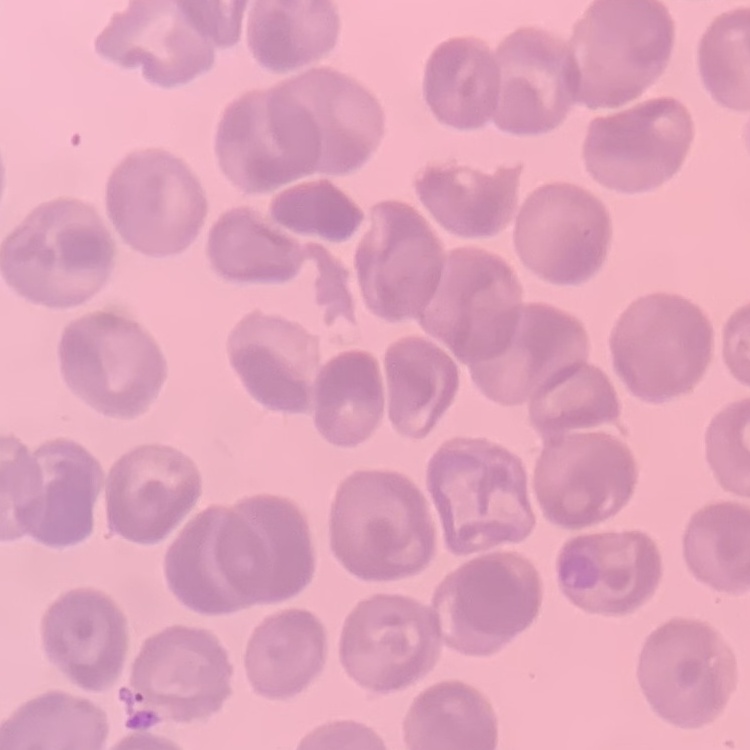

The red blood cells show no rouleaux formation. Thin blood smear. Stained with either Field's or Giemsa. One tile cut from a larger photomicrograph.